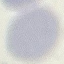

Result: no malaria parasites seen. Automatically extracted cell patch, resized to 64 × 64 pixels. Giemsa-stained preparation. Acquired by smartphone through the microscope eyepiece. Thin smear of blood.